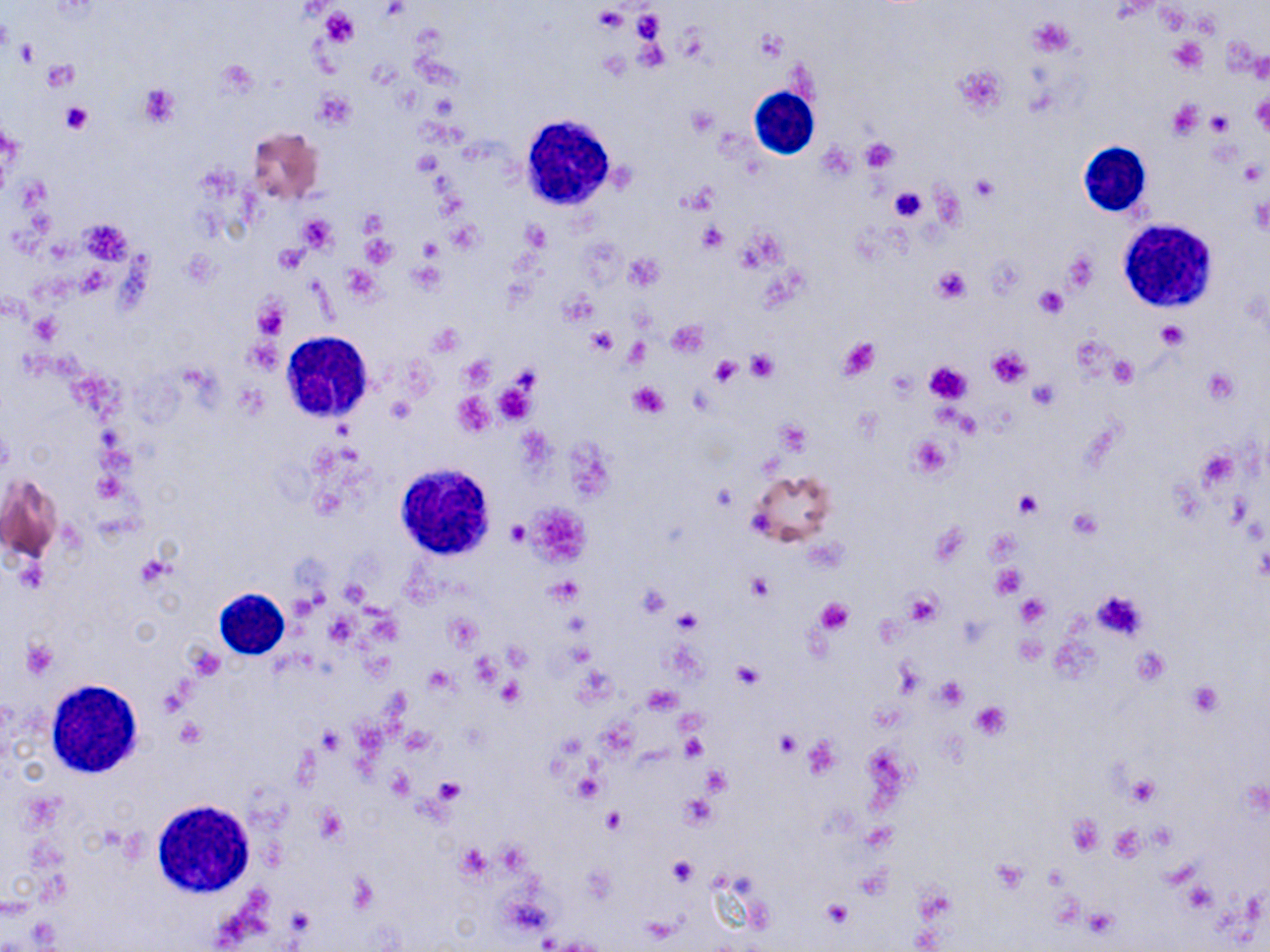

Summary:
  - Coordinate format: approximate bounding boxes as [x1, y1, x2, y2] in pixels
  - Uninfected red blood cell locations: [246, 127, 324, 205], [271, 241, 307, 276], [746, 470, 838, 549], [2, 474, 62, 566]
  - Platelet locations: [594, 6, 626, 33], [321, 9, 356, 45], [631, 9, 664, 42], [1028, 16, 1077, 56], [754, 29, 787, 64], [637, 38, 670, 70], [1168, 39, 1207, 73], [14, 40, 41, 65], [41, 62, 77, 90], [954, 64, 1006, 116], [138, 83, 181, 128], [313, 89, 357, 128], [1251, 91, 1270, 135], [1166, 98, 1203, 138], [59, 102, 94, 133], [686, 107, 717, 135], [1207, 110, 1232, 134], [862, 137, 896, 173], [411, 151, 443, 177], [1238, 159, 1265, 186], [970, 174, 998, 202], [889, 185, 926, 223], [298, 215, 336, 252], [523, 222, 549, 251], [698, 223, 725, 253], [361, 234, 395, 267], [419, 238, 444, 262], [275, 244, 306, 275], [1063, 248, 1099, 293], [624, 255, 664, 290], [931, 264, 971, 303], [1035, 286, 1066, 320], [252, 297, 290, 341], [30, 314, 59, 344], [668, 319, 708, 355], [1156, 323, 1187, 350], [587, 327, 617, 354], [623, 336, 650, 366], [837, 336, 881, 381], [986, 348, 1031, 388], [746, 351, 777, 381], [1109, 355, 1136, 386], [709, 356, 743, 383], [924, 363, 971, 404], [1202, 367, 1238, 404], [1028, 379, 1058, 409], [628, 382, 670, 418], [492, 383, 535, 426], [452, 392, 495, 436], [387, 394, 414, 423], [776, 420, 811, 455], [907, 435, 954, 479], [711, 482, 738, 510], [1014, 491, 1041, 518], [506, 521, 530, 544], [136, 555, 173, 587], [994, 565, 1026, 598], [747, 574, 772, 600], [549, 578, 581, 606], [639, 584, 670, 617], [1092, 590, 1148, 639], [904, 592, 942, 624], [1015, 595, 1048, 627], [815, 597, 854, 634], [673, 610, 700, 634], [20, 639, 59, 679], [732, 661, 763, 689], [935, 678, 966, 709], [499, 680, 524, 706], [1187, 680, 1223, 717], [969, 700, 1011, 740], [175, 717, 207, 747], [402, 726, 437, 755], [318, 727, 341, 756], [776, 732, 801, 755], [801, 734, 841, 780], [682, 737, 706, 760], [702, 765, 732, 796], [387, 767, 416, 799], [1125, 776, 1160, 808], [434, 777, 463, 802], [680, 794, 718, 828], [603, 808, 626, 833], [1068, 814, 1105, 857], [1108, 824, 1148, 862], [455, 843, 492, 881], [667, 856, 697, 886], [991, 861, 1030, 891], [1183, 883, 1214, 914], [822, 900, 852, 928], [1081, 905, 1119, 941]
  - White blood cell locations: [744, 82, 814, 165], [519, 115, 619, 209], [1079, 140, 1152, 218], [1117, 219, 1217, 314], [281, 332, 375, 422], [394, 461, 499, 559], [216, 588, 290, 659], [44, 679, 147, 779], [152, 800, 256, 896]
  - Slide-level diagnosis: no evidence of blood parasites
  - Field of view: one of a larger specimen
  - Magnification: 1000x
  - Preparation: thin blood smear
  - Modality: optical microscopy
  - Image size: 1270×952 pixels
  - Stain: May-Grünwald-Giemsa